Classify this cell by malaria status.
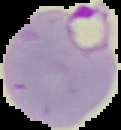

Parasitized.

preparation: thin blood film
image_type: segmented cell region on a black background
image_size: 121×130 pixels